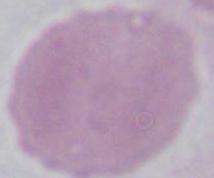

{
  "identification": "erythrocyte",
  "magnification": "1000x",
  "modality": "micrograph"
}